Identify the cell.
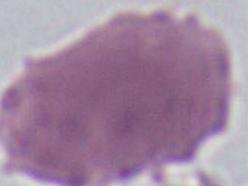

This is an erythrocyte.

Micrograph. 1000x magnification.